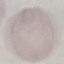
Summary:
  - Malaria status: uninfected
  - Stain: Giemsa
  - Preparation: thin blood film
  - Capture: smartphone through the microscope eyepiece
  - Image type: automatically extracted cell patch, resized to 64 × 64 pixels